Report the malaria status of this cell.
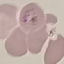
Uninfected.

Summary:
  - Preparation: thin smear
  - Stain: Giemsa
  - Image type: cell patch, automatically extracted from a larger field of view and resized to 64 × 64 pixels
  - Capture: smartphone through the microscope eyepiece